State which cell type is depicted.
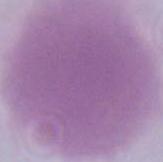
An erythrocyte.

modality = photomicrograph
magnification = 1000x